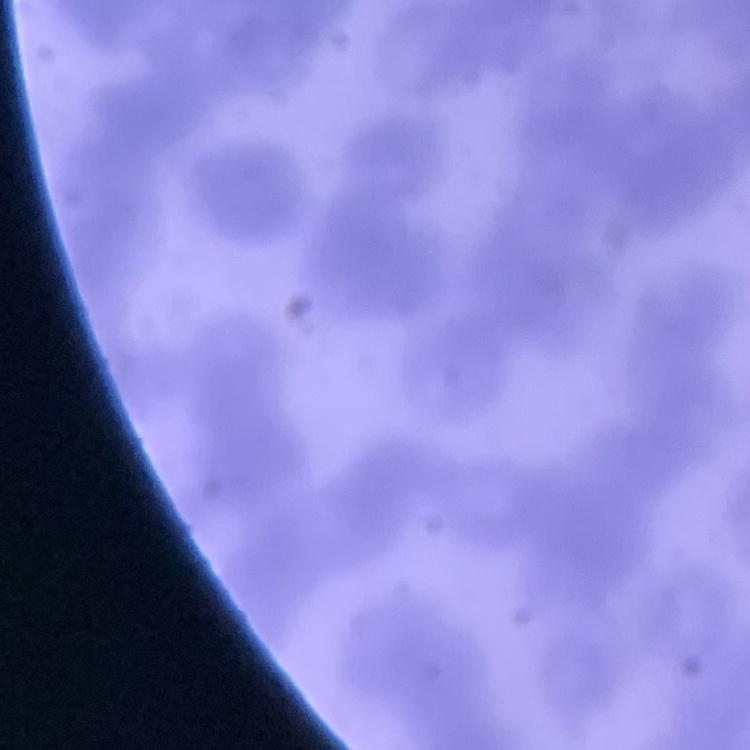

Summary:
  - Red blood cell morphology: rouleaux formation
  - Preparation: thin peripheral smear
  - Image type: square crop of a larger photomicrograph
  - Stain: Field's or Giemsa